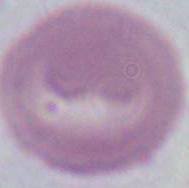

Summary:
  - Modality: micrograph
  - Magnification: 1000x
  - Identification: red blood cell